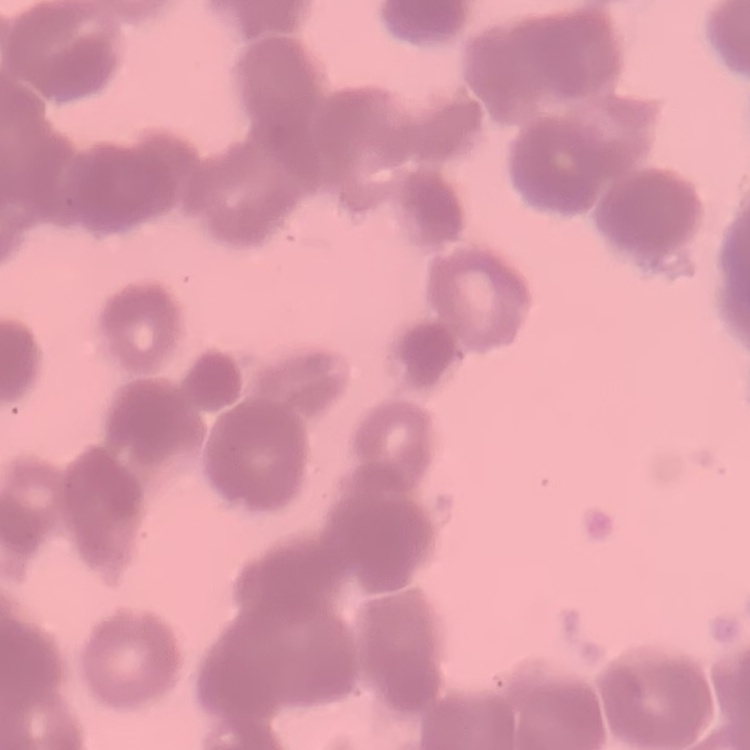

Summary:
  - Erythrocyte morphology: rouleaux formation
  - Stain: Field's or Giemsa
  - Preparation: thin peripheral smear
  - Image type: one tile cut from a larger photomicrograph